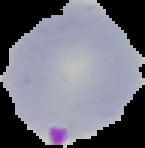
Summary:
  - Image size: 145×148 pixels
  - Malaria status: parasitized
  - Image type: cell region segmented out of the field of view; surrounding area masked to black
  - Preparation: thin blood film